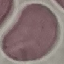

result = no malaria parasites seen
stain = Giemsa
image type = automatically extracted cell patch, resized to 64 × 64 pixels
capture = smartphone camera at the microscope eyepiece
preparation = thin blood film